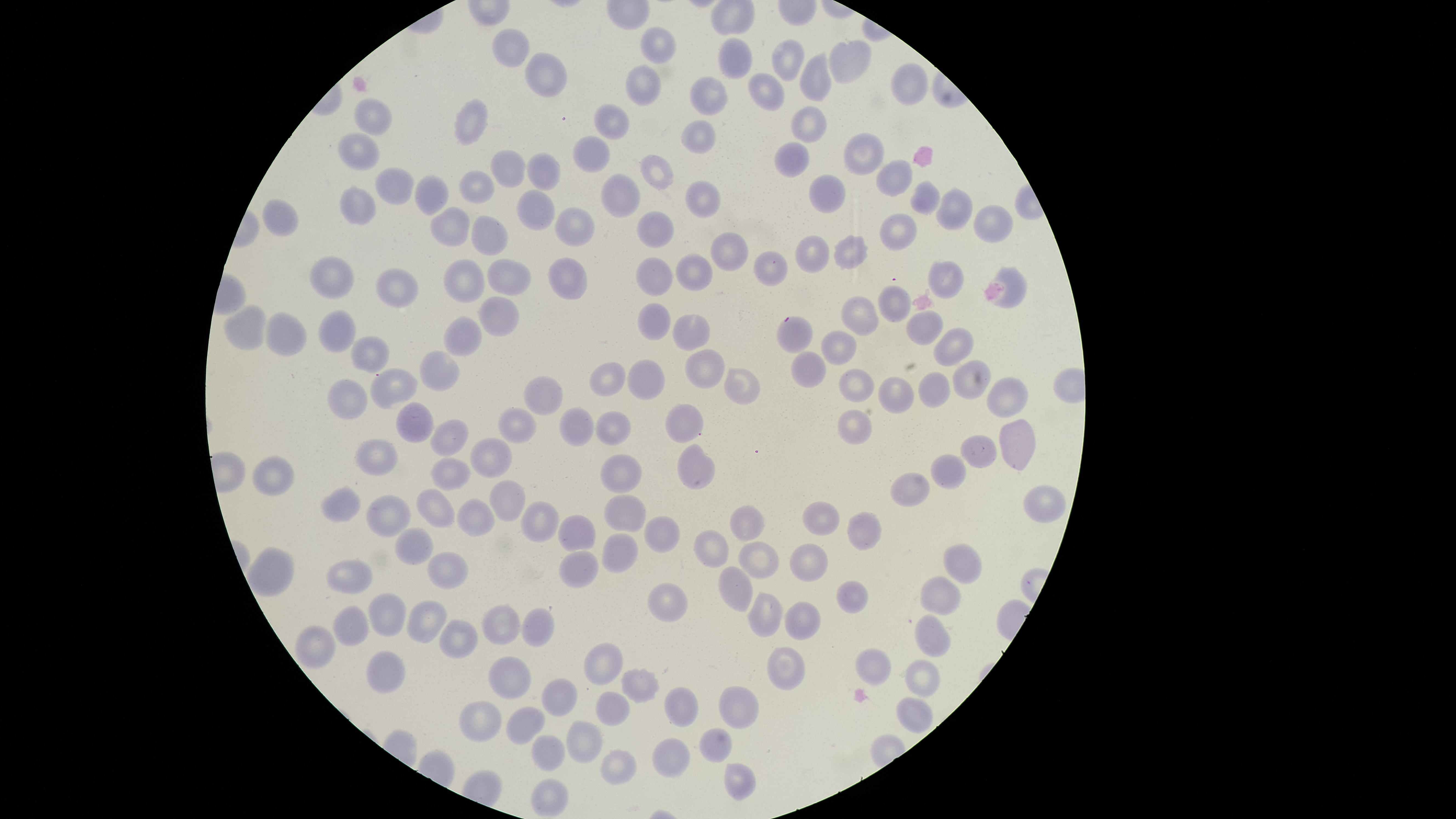

image size = 1456×819 pixels
uninfected red blood cells = approximate marker points as [x, y] in pixels: [657, 42], [508, 50], [791, 58], [737, 60], [845, 65], [817, 74], [545, 79], [642, 83], [913, 83], [765, 90], [708, 95], [616, 115], [372, 116], [473, 124], [805, 124], [697, 130], [859, 151], [361, 152], [593, 154], [795, 154], [512, 169], [543, 169], [660, 173], [888, 179], [828, 184], [482, 186], [395, 187], [619, 191], [430, 196], [926, 199], [700, 202], [357, 208], [949, 208], [533, 211], [278, 219], [453, 222], [992, 222], [576, 225], [661, 225], [906, 230], [488, 232], [859, 245], [723, 250], [815, 252], [771, 263], [659, 270], [685, 271], [510, 273], [468, 275], [947, 277], [565, 278], [336, 279], [1014, 279], [399, 289], [895, 303], [858, 315], [499, 317], [658, 319], [247, 327], [922, 327], [335, 330], [688, 330], [797, 333], [468, 334], [284, 335], [953, 343], [836, 346], [370, 354], [443, 365], [807, 365], [704, 368], [611, 374], [657, 376], [734, 379], [969, 380], [858, 383], [390, 385], [894, 390], [931, 390], [1002, 395], [548, 399], [352, 402], [409, 419], [679, 422], [518, 424], [856, 424], [575, 425], [616, 425], [461, 436], [1014, 450], [490, 457], [978, 459], [377, 461], [622, 472], [690, 472], [949, 473], [274, 478], [445, 478], [911, 485], [498, 500], [1042, 502], [434, 505], [344, 506], [621, 508], [389, 512], [470, 516], [820, 518], [542, 521], [747, 522], [576, 530], [867, 532], [660, 537], [420, 540], [712, 547], [623, 549], [761, 560], [806, 563], [965, 563], [271, 567], [578, 567], [446, 571], [351, 579], [733, 591], [854, 594], [940, 598], [670, 606], [768, 610], [394, 613], [427, 620], [537, 620], [805, 620], [500, 623], [355, 626], [461, 630], [934, 642], [317, 647], [610, 659], [875, 662], [390, 669], [782, 673], [512, 679], [926, 681], [641, 684], [556, 698], [613, 708], [677, 708], [738, 712], [914, 712], [487, 719], [528, 724], [587, 739], [718, 742], [552, 757], [669, 758], [621, 767], [733, 779], [550, 797]
visible region = circular
preparation = thin blood film
presence = no malaria parasites detected
capture = smartphone photograph through the microscope eyepiece
field of view = single
stain = Giemsa